Locate every Plasmodium parasite.
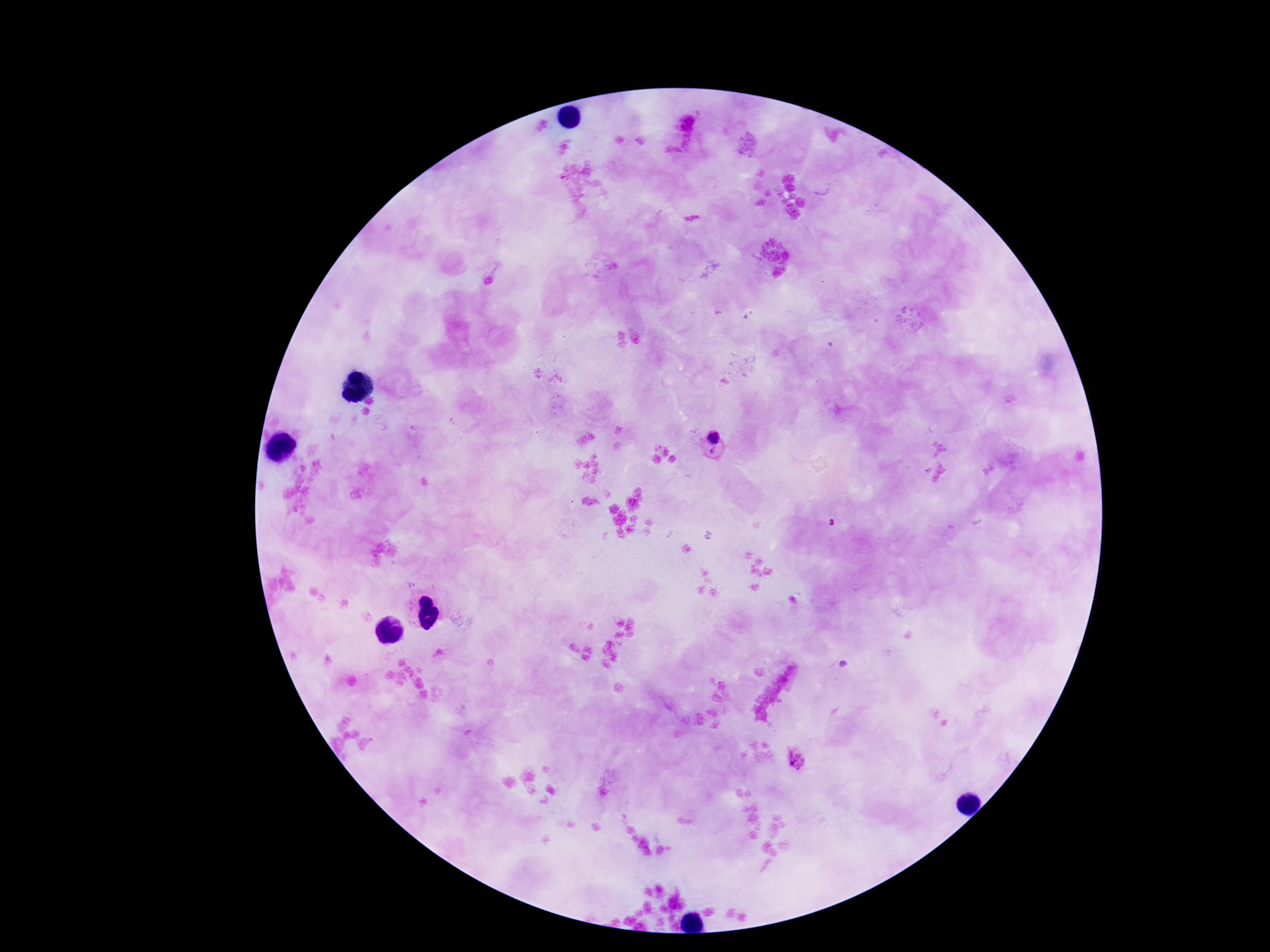

Approximate object centers, in pixels from the top-left corner.
Plasmodium parasites: (x=713, y=445), (x=797, y=759).

{
  "patient_malaria_status": "infected",
  "capture": "smartphone camera through the microscope eyepiece",
  "field_of_view": "one from this slide",
  "preparation": "thick blood film",
  "image_size": "1270×952 pixels",
  "magnification": "100x",
  "stain": "Giemsa"
}